Classify this cell by malaria status.
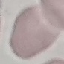
Uninfected.

stain: Giemsa
preparation: thin blood film
capture: smartphone camera at the microscope eyepiece
image_type: automatically extracted cell patch, resized to 64 × 64 pixels